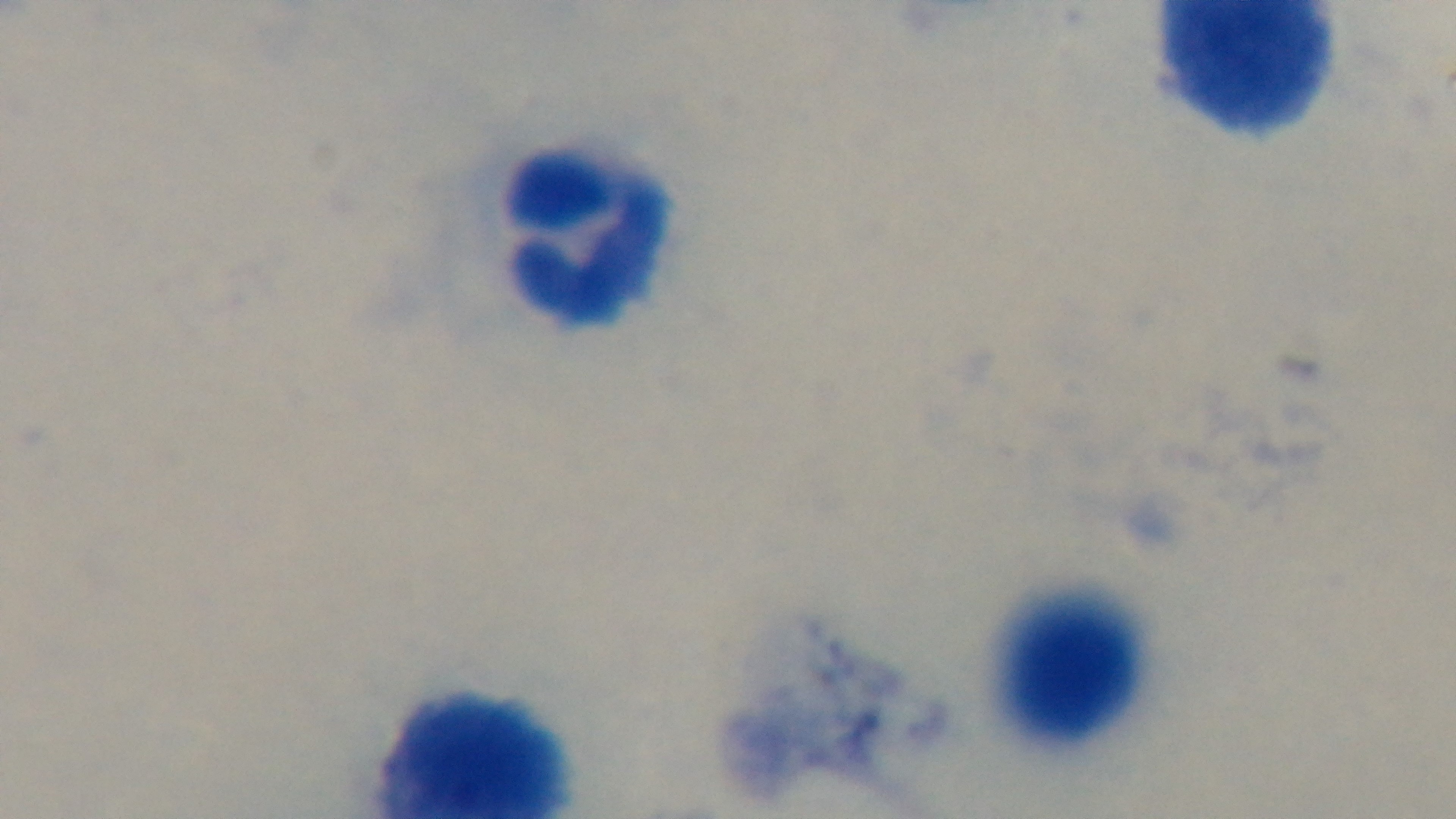

Summary:
  - Capture: mounted 4K digital camera
  - Field of view: one from the slide
  - Malaria status: negative
  - Modality: light microscopy
  - Stain: Giemsa
  - Objective: 100x oil immersion
  - Preparation: thick smear